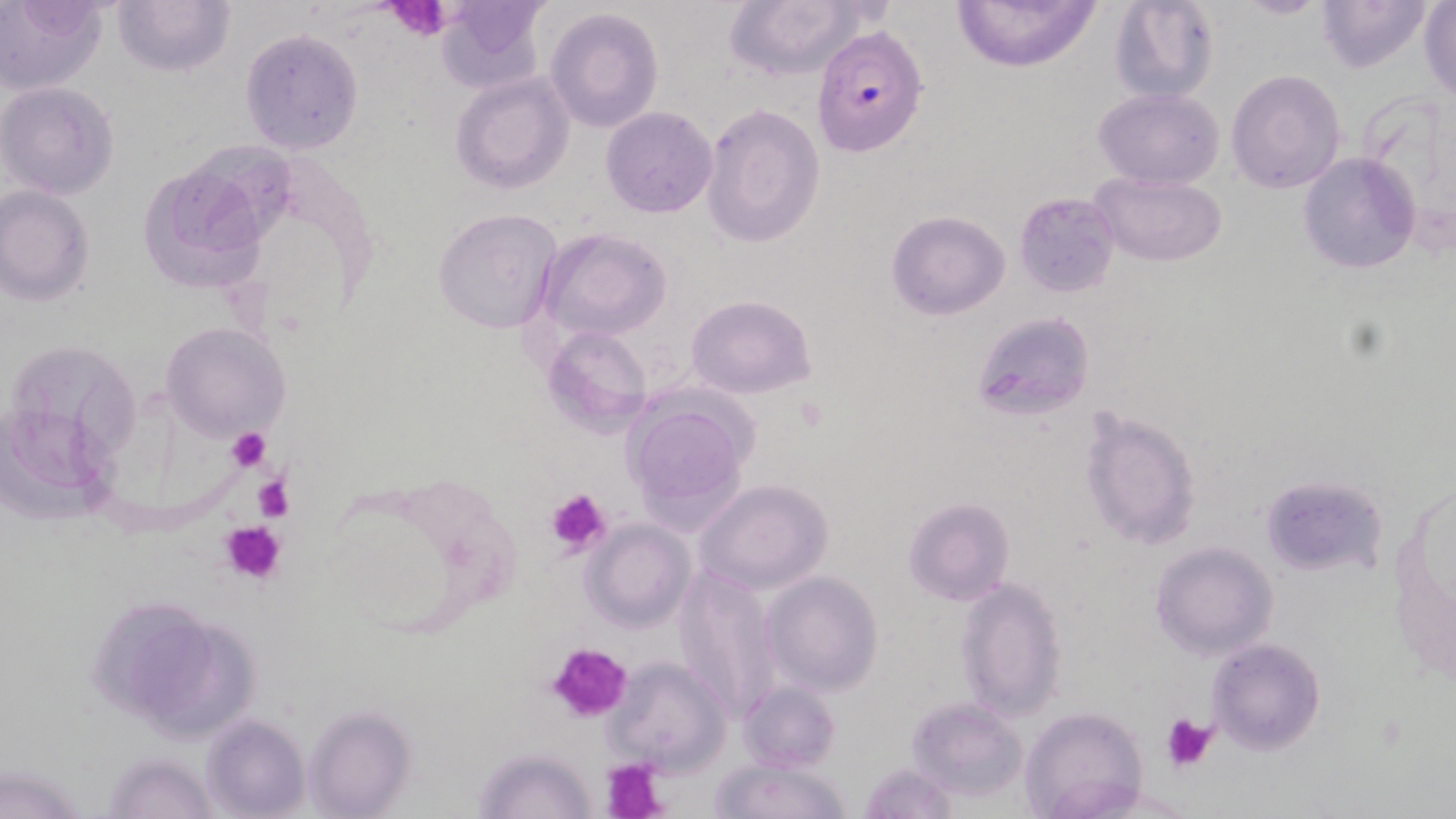

slide-level diagnosis = Plasmodium falciparum
field of view = one of a larger specimen
Plasmodium falciparum-infected red blood cell locations = approximate bounding boxes as (x1,y1)-(x2,y2) corner pairs in pixels: (810,24)-(928,158)
uninfected red blood cell locations = approximate bounding boxes as (x1,y1)-(x2,y2) corner pairs in pixels: (1,0)-(107,93), (111,0)-(235,77), (433,0)-(550,93), (723,0)-(869,81), (951,0)-(1100,70), (1107,0)-(1220,106), (1234,0)-(1329,19), (1315,0)-(1433,73), (1419,3)-(1455,102), (546,7)-(665,134), (239,28)-(364,156), (1226,70)-(1346,192), (450,72)-(575,193), (1,81)-(121,200), (1093,87)-(1224,189), (700,102)-(826,249), (601,106)-(718,218), (1298,153)-(1421,275), (136,156)-(272,295), (1088,171)-(1228,267), (0,185)-(95,306), (1014,192)-(1121,298), (432,208)-(563,334), (886,210)-(1011,319), (536,226)-(672,343), (685,293)-(817,399), (970,311)-(1096,421), (161,321)-(291,441), (540,327)-(652,435), (16,336)-(138,464), (621,396)-(752,529), (5,406)-(121,532), (1080,408)-(1202,549), (1386,464)-(1454,688), (1259,475)-(1386,576), (693,479)-(835,595), (903,497)-(1014,605), (582,520)-(694,633), (1149,541)-(1278,660), (671,562)-(785,720), (762,570)-(884,697), (954,576)-(1067,723), (87,598)-(213,715), (129,618)-(261,740), (1207,637)-(1325,754), (604,655)-(732,776), (735,679)-(840,773), (905,697)-(1027,802), (301,706)-(415,817), (1018,706)-(1146,818), (202,714)-(309,819), (474,744)-(600,819), (103,751)-(216,819), (710,754)-(853,819), (859,761)-(960,818)
platelet locations = approximate bounding boxes as (x1,y1)-(x2,y2) corner pairs in pixels: (382,1)-(457,40), (796,394)-(830,433), (225,428)-(272,472), (254,475)-(293,522), (544,488)-(613,557), (222,519)-(285,586), (544,641)-(633,725), (1161,712)-(1218,773), (603,757)-(668,819)
image size = 1456×819 pixels
stain = May-Grünwald-Giemsa
magnification = 1000x
modality = light microscopy
preparation = thin blood film